Identify the preparation type.
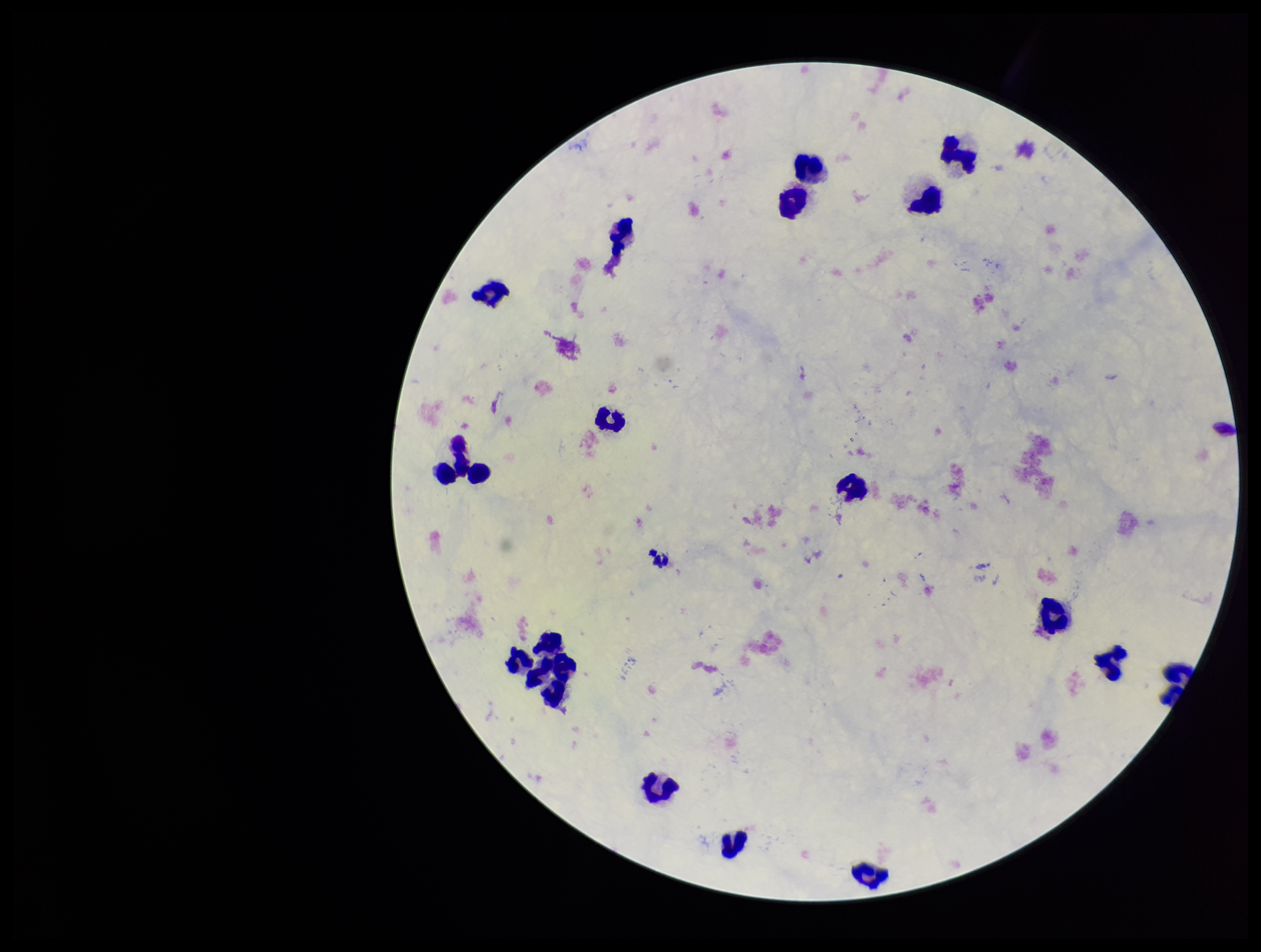
It is a thick blood smear.

Summary:
  - Parasite count: 0
  - Capture: smartphone photograph through the microscope eyepiece
  - Patient malaria status: negative
  - Stain: Giemsa
  - Plasmodium parasites: none seen
  - Image size: 1261×952 pixels
  - Leukocyte count: 19
  - Field of view: one from this slide